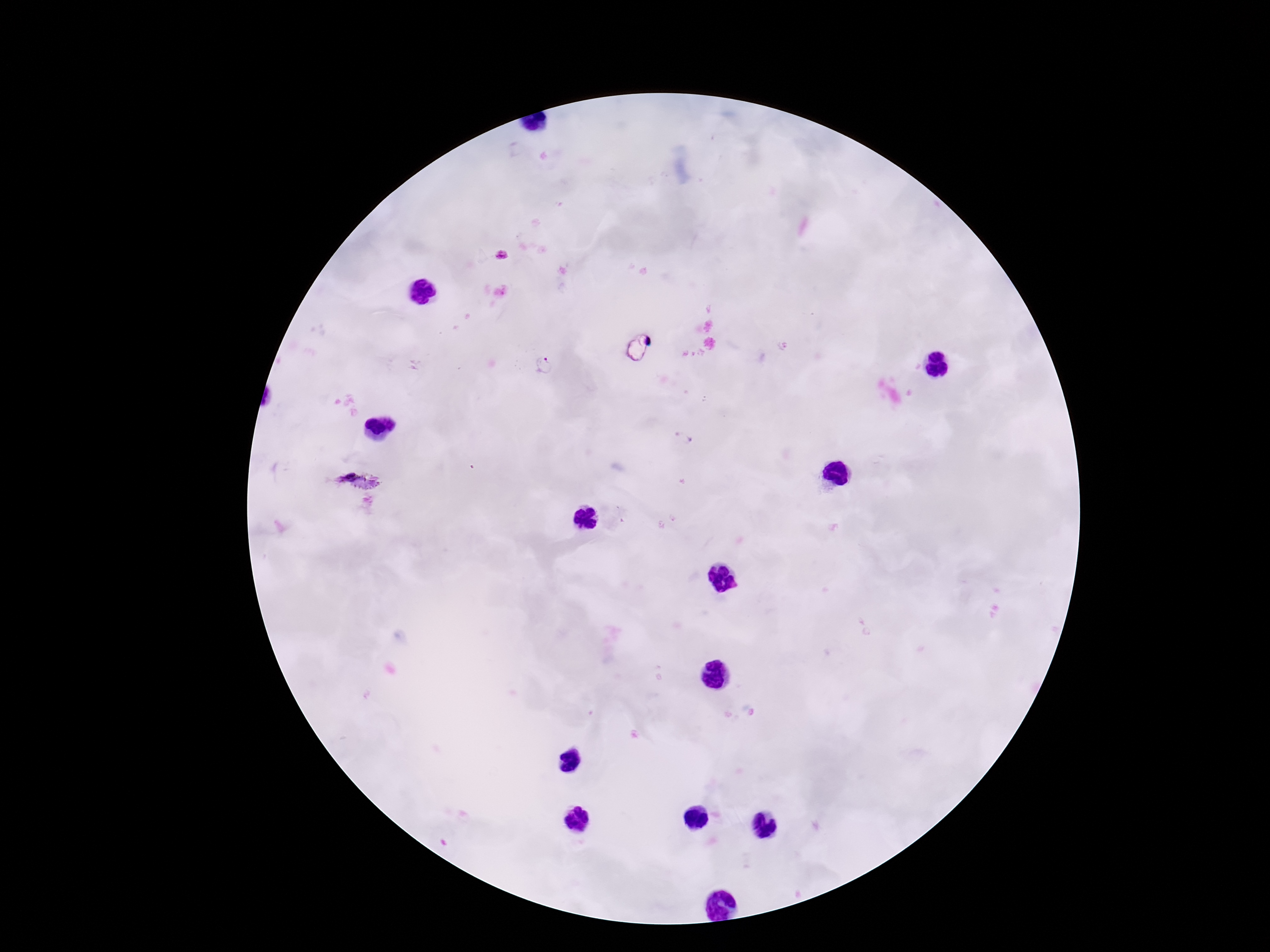 Approximate object centers, in pixels from the top-left corner. Plasmodium parasite locations: (x=544, y=366), (x=683, y=439), (x=347, y=476). Giemsa stain. Image is 1270×952 pixels. Thick blood film. 100x magnification. Patient malaria status: infected. One field from this slide. Smartphone photograph taken through the microscope eyepiece.